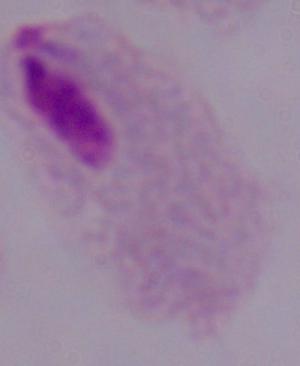
A trichomonad is seen. Micrograph. Captured at 1000x magnification.